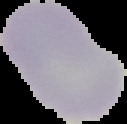
Malaria status: uninfected. The area outside the segmented cell region is set to black. From a thin blood smear. Image is 127×124 pixels.